Report the malaria status of this cell.
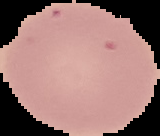

Uninfected.

Summary:
  - Image size: 160×136 pixels
  - Image type: segmented cell region with the area outside set to black
  - Preparation: thin blood smear